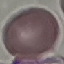 Result: no malaria parasites seen. Automatically extracted cell patch, resized to 64 × 64 pixels. Giemsa-stained preparation. Photographed with a smartphone camera at the microscope eyepiece. Thin blood film.